Name the parasite shown.
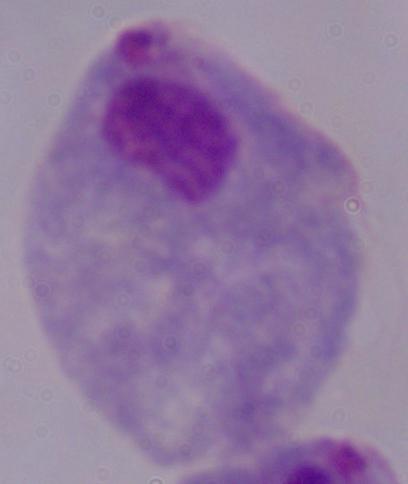
A trichomonad.

magnification: 1000x
modality: micrograph